Identify the parasite.
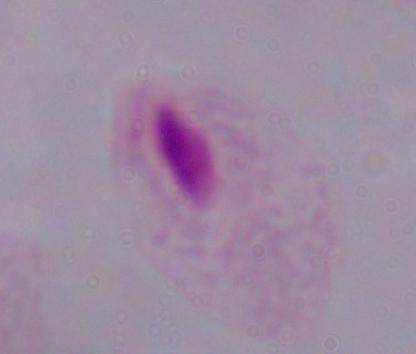

This is a trichomonad.

Micrograph. Captured at 1000x magnification.